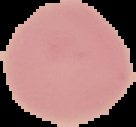
image size = 136×127 pixels
image type = segmented cell region on a black background
preparation = thin blood smear
result = no Plasmodium parasites detected